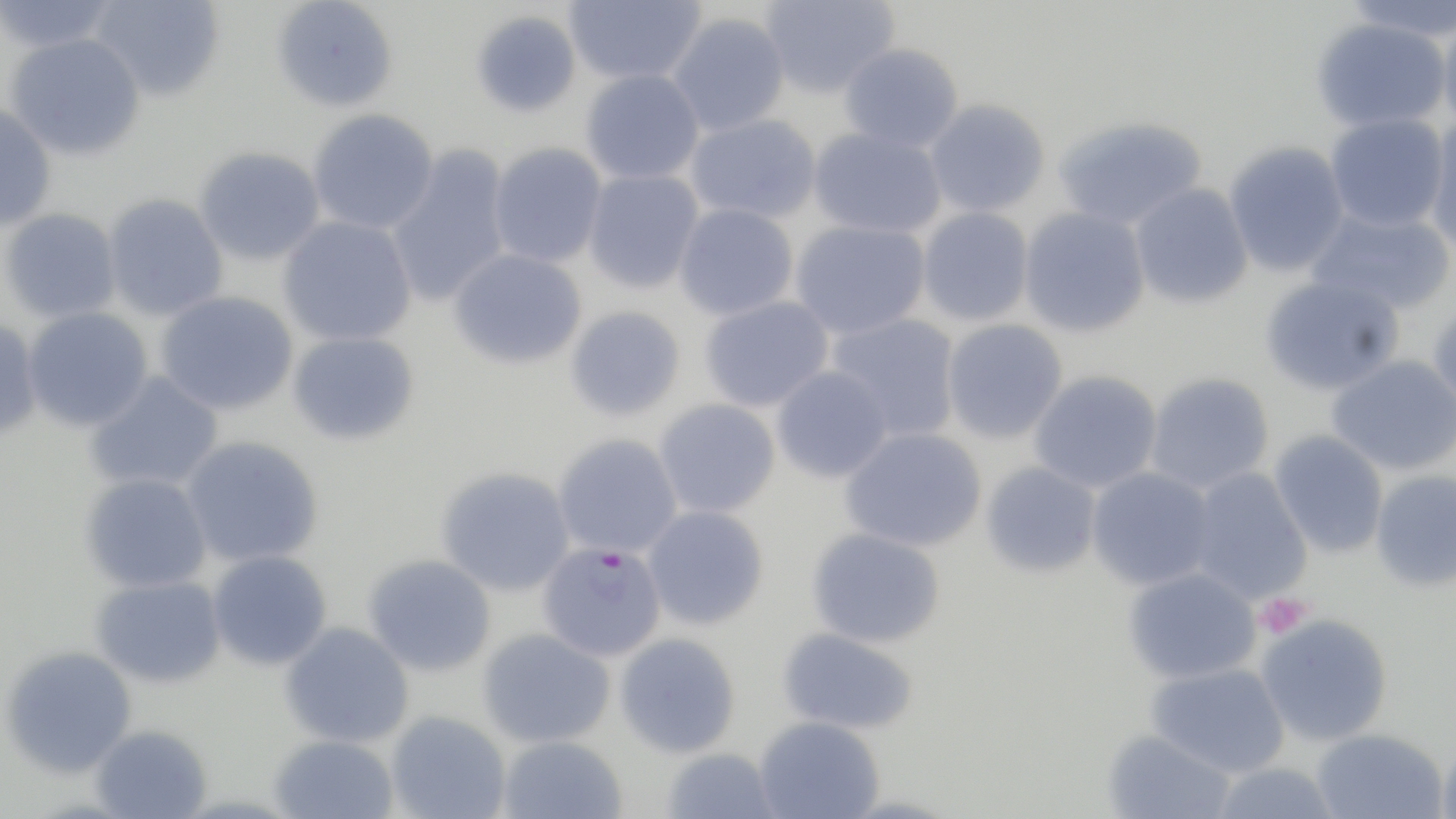
Approximate bounding boxes as [x1, y1, x2, y2] in pixels. Platelet locations: [1255, 593, 1311, 639]. Uninfected red blood cell locations: [0, 0, 124, 53], [90, 0, 225, 103], [271, 0, 399, 113], [563, 0, 706, 85], [760, 0, 899, 100], [1343, 0, 1456, 42], [470, 9, 582, 119], [1437, 12, 1456, 134], [667, 13, 790, 136], [1312, 17, 1451, 132], [5, 33, 145, 161], [838, 43, 964, 153], [580, 69, 705, 185], [924, 99, 1050, 217], [0, 103, 57, 232], [308, 109, 439, 234], [685, 113, 821, 223], [1324, 114, 1449, 232], [1053, 116, 1208, 231], [1423, 119, 1456, 257], [808, 127, 947, 238], [1223, 141, 1350, 277], [488, 142, 607, 267], [386, 143, 514, 306], [193, 147, 325, 266], [582, 168, 704, 294], [1129, 183, 1253, 309], [102, 193, 228, 322], [674, 203, 799, 320], [1304, 204, 1455, 315], [1018, 206, 1151, 338], [917, 207, 1034, 326], [0, 208, 122, 323], [278, 215, 417, 346], [790, 219, 931, 340], [448, 248, 587, 370], [1259, 275, 1405, 397], [156, 290, 298, 416], [699, 295, 834, 412], [1428, 298, 1456, 417], [21, 306, 154, 432], [565, 306, 685, 421], [826, 312, 962, 440], [0, 317, 42, 440], [941, 318, 1068, 444], [286, 331, 421, 446], [1326, 354, 1456, 476], [771, 365, 893, 484], [1029, 370, 1163, 493], [83, 371, 224, 493], [1145, 372, 1275, 494], [654, 398, 781, 518], [840, 426, 987, 552], [1269, 429, 1389, 558], [553, 433, 683, 559], [181, 435, 324, 567], [979, 461, 1102, 579], [435, 466, 575, 596], [1085, 466, 1218, 591], [1185, 466, 1313, 605], [1370, 469, 1456, 592], [79, 472, 212, 593], [641, 505, 770, 630], [806, 527, 945, 648], [207, 550, 332, 671], [362, 554, 497, 676], [1122, 566, 1261, 684], [90, 575, 227, 688], [1256, 613, 1394, 746], [280, 622, 414, 748], [777, 627, 919, 735], [478, 628, 615, 748], [614, 632, 741, 758], [1, 645, 136, 778], [1146, 662, 1290, 777], [385, 709, 511, 819], [754, 716, 884, 819], [90, 724, 212, 818], [1310, 728, 1448, 819], [1101, 729, 1236, 818], [267, 734, 399, 819], [497, 735, 628, 819], [1438, 736, 1456, 819], [661, 747, 781, 819], [1209, 761, 1343, 819]. Plasmodium falciparum-infected red blood cell locations: [537, 541, 667, 662]. Slide-level diagnosis: Plasmodium falciparum. Single field of view. Optical microscopy. May-Grünwald-Giemsa stain. 1000x magnification. Thin blood smear. Image is 1456×819 pixels.